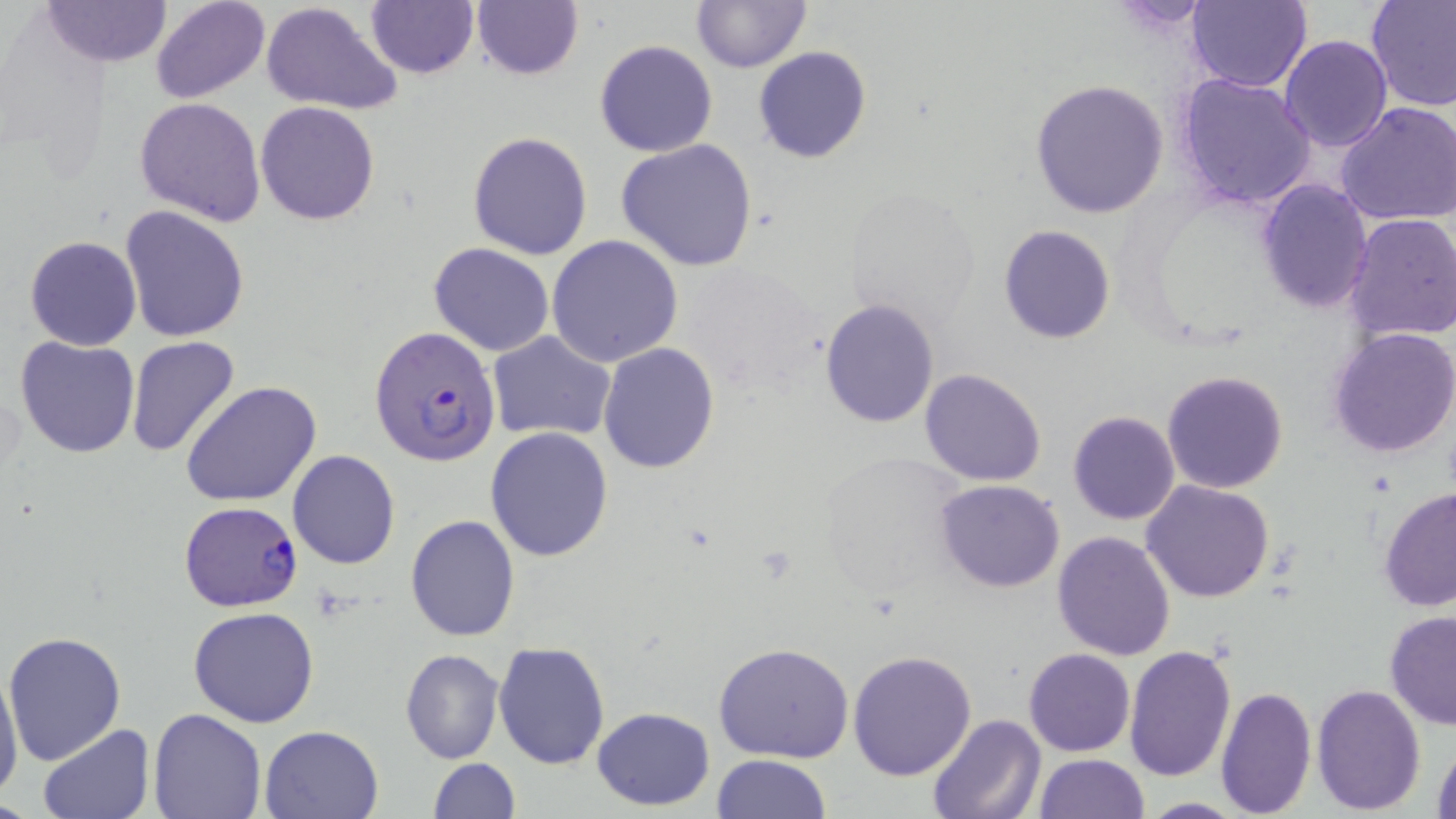

slide_level_diagnosis: Plasmodium falciparum
magnification: 1000x
image_size: 1456×819 pixels
plasmodium_falciparum_infected_red_blood_cell_locations: 'approximate bounding boxes as (x1,y1)-(x2,y2) corner pairs in pixels: (369,325)-(501,468), (177,501)-(303,612)'
field_of_view: single
uninfected_red_blood_cell_locations: 'approximate bounding boxes as (x1,y1)-(x2,y2) corner pairs in pixels: (40,0)-(171,68), (150,0)-(271,104), (366,0)-(479,79), (1186,0)-(1310,93), (1365,0)-(1456,112), (259,1)-(404,116), (470,1)-(584,81), (692,1)-(810,73), (1280,34)-(1392,152), (595,39)-(718,158), (753,46)-(872,163), (1203,55)-(1378,186), (1176,74)-(1317,210), (1028,78)-(1171,219), (135,96)-(266,225), (255,101)-(380,226), (1335,101)-(1456,226), (468,131)-(595,260), (616,138)-(758,272), (1257,179)-(1373,314), (119,203)-(252,342), (1343,213)-(1456,344), (998,224)-(1116,344), (25,235)-(141,351), (548,235)-(683,368), (428,243)-(555,356), (820,299)-(940,428), (1328,327)-(1456,461), (486,330)-(617,442), (127,336)-(240,457), (15,337)-(139,458), (599,342)-(720,473), (918,367)-(1047,488), (1161,370)-(1289,494), (181,381)-(321,506), (1067,410)-(1181,526), (486,427)-(614,561), (812,450)-(973,606), (288,451)-(400,569), (936,479)-(1065,593), (1141,481)-(1276,604), (1379,487)-(1456,612), (404,515)-(521,642), (1052,530)-(1177,660), (189,606)-(320,729), (1384,611)-(1456,731), (4,630)-(127,764), (494,642)-(610,769), (713,642)-(854,763), (1123,643)-(1237,782), (1024,647)-(1135,757), (399,648)-(503,764), (847,648)-(978,779), (0,658)-(25,808), (1311,682)-(1427,814), (1214,684)-(1316,817), (148,707)-(267,819), (591,707)-(715,810), (926,713)-(1046,819), (39,724)-(154,818), (260,724)-(385,817), (1431,733)-(1456,819), (713,753)-(832,818), (1032,754)-(1149,818), (428,758)-(518,818), (1134,798)-(1249,817)'
modality: light microscopy
preparation: thin blood film
stain: May-Grünwald-Giemsa